Outline each blood parasite and name the species.
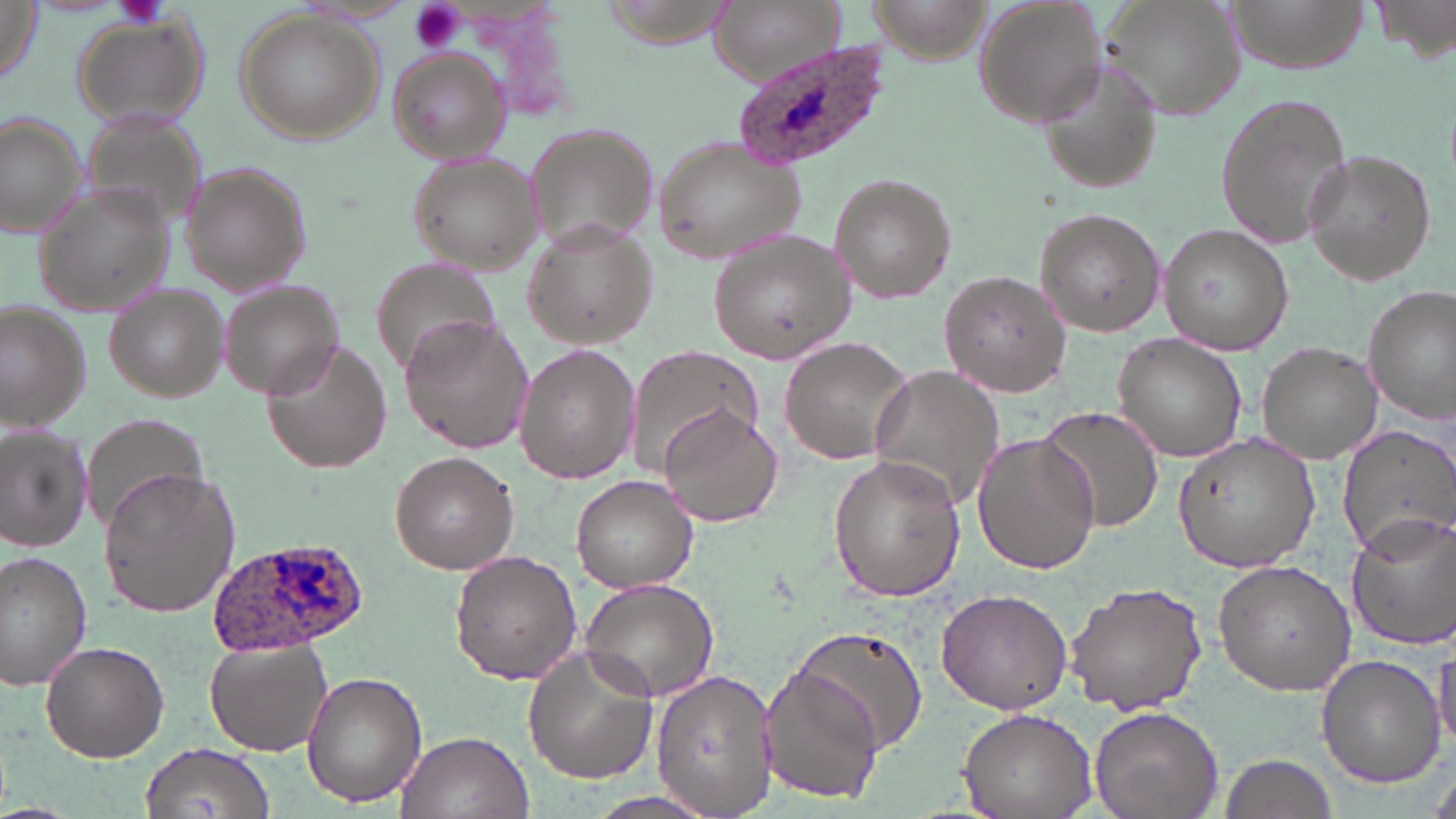
Approximate bounding boxes as (x1,y1)-(x2,y2) corner pairs in pixels.
Plasmodium ovale-infected red blood cells: (737,44)-(897,173), (208,538)-(375,654).
No Plasmodium falciparum, Plasmodium malariae, Plasmodium vivax, Babesia divergens, or Trypanosoma brucei observed.

Summary:
  - Uninfected red blood cell locations: (0,0)-(45,85), (715,0)-(840,80), (865,0)-(990,64), (974,0)-(1106,127), (1095,0)-(1244,123), (1224,0)-(1366,73), (1370,0)-(1456,61), (234,10)-(383,144), (68,14)-(208,133), (387,48)-(512,165), (1035,58)-(1167,196), (1212,92)-(1355,252), (1,113)-(88,240), (522,122)-(658,251), (651,137)-(808,263), (1302,148)-(1438,286), (407,154)-(545,276), (180,166)-(312,296), (828,171)-(956,306), (34,186)-(175,314), (1033,208)-(1167,337), (522,218)-(659,350), (1160,225)-(1291,357), (708,229)-(854,364), (371,256)-(503,382), (939,270)-(1071,398), (219,279)-(345,398), (102,285)-(229,402), (1364,285)-(1456,424), (0,303)-(90,428), (398,316)-(533,453), (1110,333)-(1247,464), (778,336)-(916,464), (261,340)-(392,475), (1255,342)-(1383,464), (513,345)-(640,483), (628,345)-(763,471), (868,365)-(1008,512), (1035,405)-(1165,535), (657,407)-(782,528), (77,414)-(209,531), (1335,421)-(1456,554), (0,424)-(93,551), (971,432)-(1101,575), (1170,432)-(1322,574), (390,450)-(518,572), (827,456)-(966,602), (98,468)-(243,617), (571,475)-(697,594), (1343,512)-(1456,651), (449,550)-(582,685), (0,551)-(95,691), (1212,559)-(1357,694), (578,576)-(719,700), (1065,582)-(1208,718), (937,587)-(1072,715), (793,625)-(931,754), (205,638)-(333,755), (40,640)-(170,762), (1431,640)-(1456,759), (523,645)-(659,783), (1316,654)-(1447,787), (759,664)-(884,807), (650,667)-(780,818), (303,670)-(425,808), (1089,706)-(1224,819), (958,708)-(1096,819), (395,729)-(533,819), (142,740)-(276,818), (1217,750)-(1339,819), (585,789)-(719,819)
  - Platelet locations: (115,0)-(170,29), (407,0)-(467,53)
  - Slide-level diagnosis: Plasmodium ovale
  - Image size: 1456×819 pixels
  - Magnification: 1000x
  - Stain: May-Grünwald-Giemsa
  - Modality: light microscopy
  - Preparation: thin blood smear
  - Field of view: one of a larger specimen